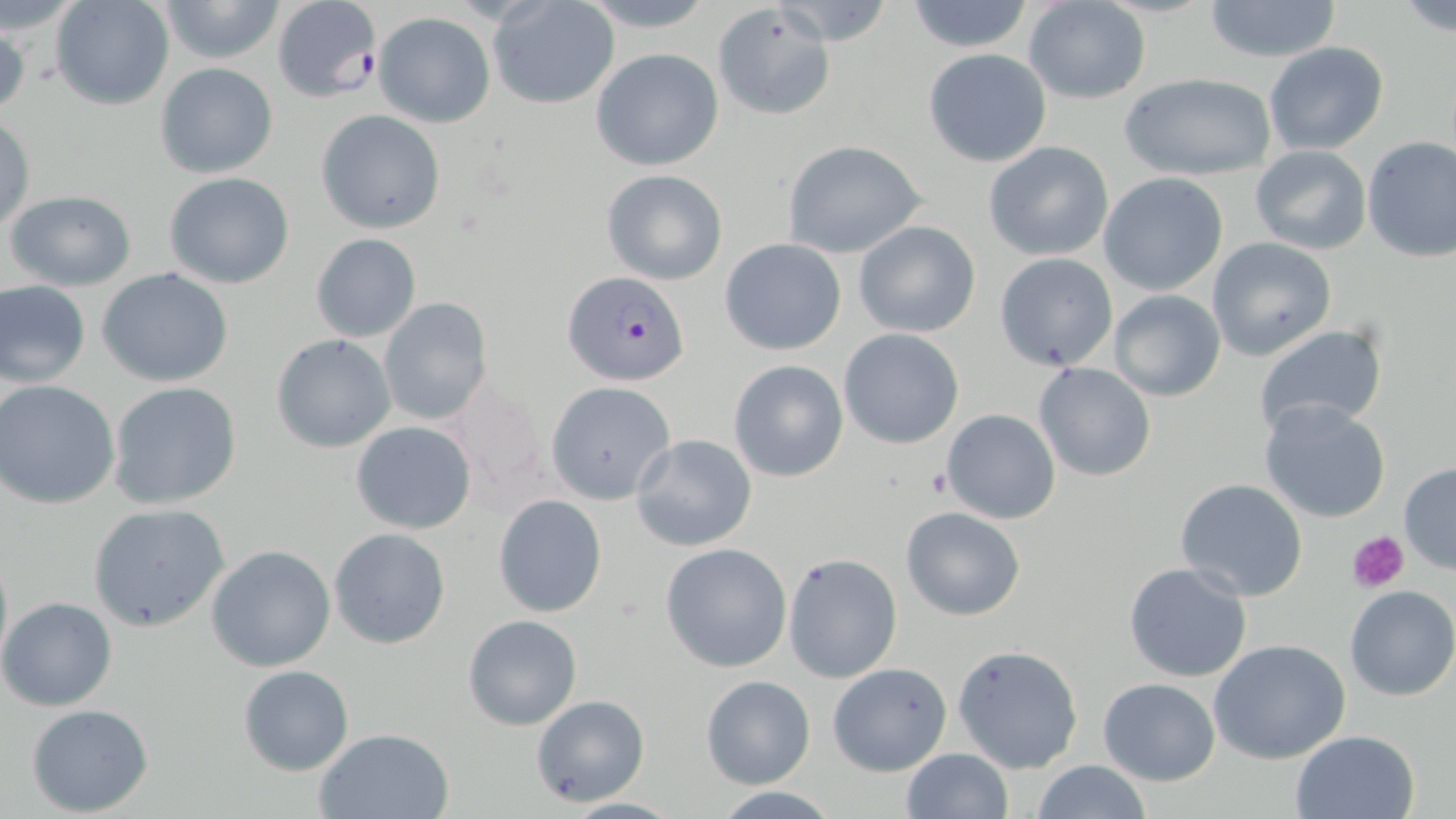

Plasmodium falciparum-infected red blood cell locations = approximate bounding boxes as (x1,y1)-(x2,y2) corner pairs in pixels: (269,2)-(384,104), (562,271)-(689,386)
slide-level diagnosis = Plasmodium falciparum
field of view = one of a larger specimen
magnification = 1000x
uninfected red blood cell locations = approximate bounding boxes as (x1,y1)-(x2,y2) corner pairs in pixels: (51,0)-(174,110), (156,0)-(288,64), (580,0)-(718,30), (902,0)-(1037,53), (487,1)-(620,109), (769,1)-(898,46), (1200,1)-(1345,62), (1391,1)-(1455,37), (1023,2)-(1152,104), (710,5)-(837,122), (373,11)-(494,128), (1,16)-(29,119), (1263,41)-(1389,157), (590,47)-(725,172), (923,47)-(1051,166), (154,62)-(279,180), (1119,71)-(1278,182), (317,109)-(445,234), (0,114)-(35,233), (1361,136)-(1456,262), (783,138)-(929,258), (984,141)-(1114,261), (1249,146)-(1372,255), (601,169)-(728,285), (162,172)-(294,289), (1099,172)-(1229,296), (4,190)-(138,291), (853,221)-(981,336), (311,232)-(421,343), (1206,236)-(1336,361), (719,239)-(846,356), (994,253)-(1119,372), (100,269)-(234,387), (0,280)-(91,387), (1109,290)-(1226,402), (378,297)-(492,427), (1251,324)-(1390,441), (838,329)-(965,448), (271,335)-(396,453), (728,360)-(848,482), (1034,363)-(1156,482), (544,380)-(677,503), (0,381)-(120,509), (107,381)-(242,510), (445,381)-(554,508), (1259,399)-(1392,523), (941,408)-(1061,525), (351,421)-(476,534), (631,433)-(757,552), (1397,462)-(1456,574), (1174,479)-(1308,602), (493,493)-(608,616), (88,502)-(229,631), (900,505)-(1027,620), (328,526)-(452,649), (0,541)-(12,675), (660,542)-(793,673), (206,545)-(335,672), (783,552)-(902,682), (1123,561)-(1254,683), (1344,585)-(1456,702), (0,597)-(118,712), (463,613)-(582,729), (1208,639)-(1354,764), (951,643)-(1083,774), (827,663)-(951,776), (238,664)-(353,775), (700,674)-(816,788), (1098,677)-(1220,785), (530,693)-(649,807), (27,704)-(155,816), (314,727)-(453,818), (1289,729)-(1421,819), (902,748)-(1012,818), (1032,760)-(1152,819), (707,787)-(845,817), (554,796)-(686,818)
image size = 1456×819 pixels
platelet locations = approximate bounding boxes as (x1,y1)-(x2,y2) corner pairs in pixels: (924,468)-(955,499), (1348,531)-(1410,595)
stain = May-Grünwald-Giemsa
modality = optical microscopy
preparation = thin blood smear